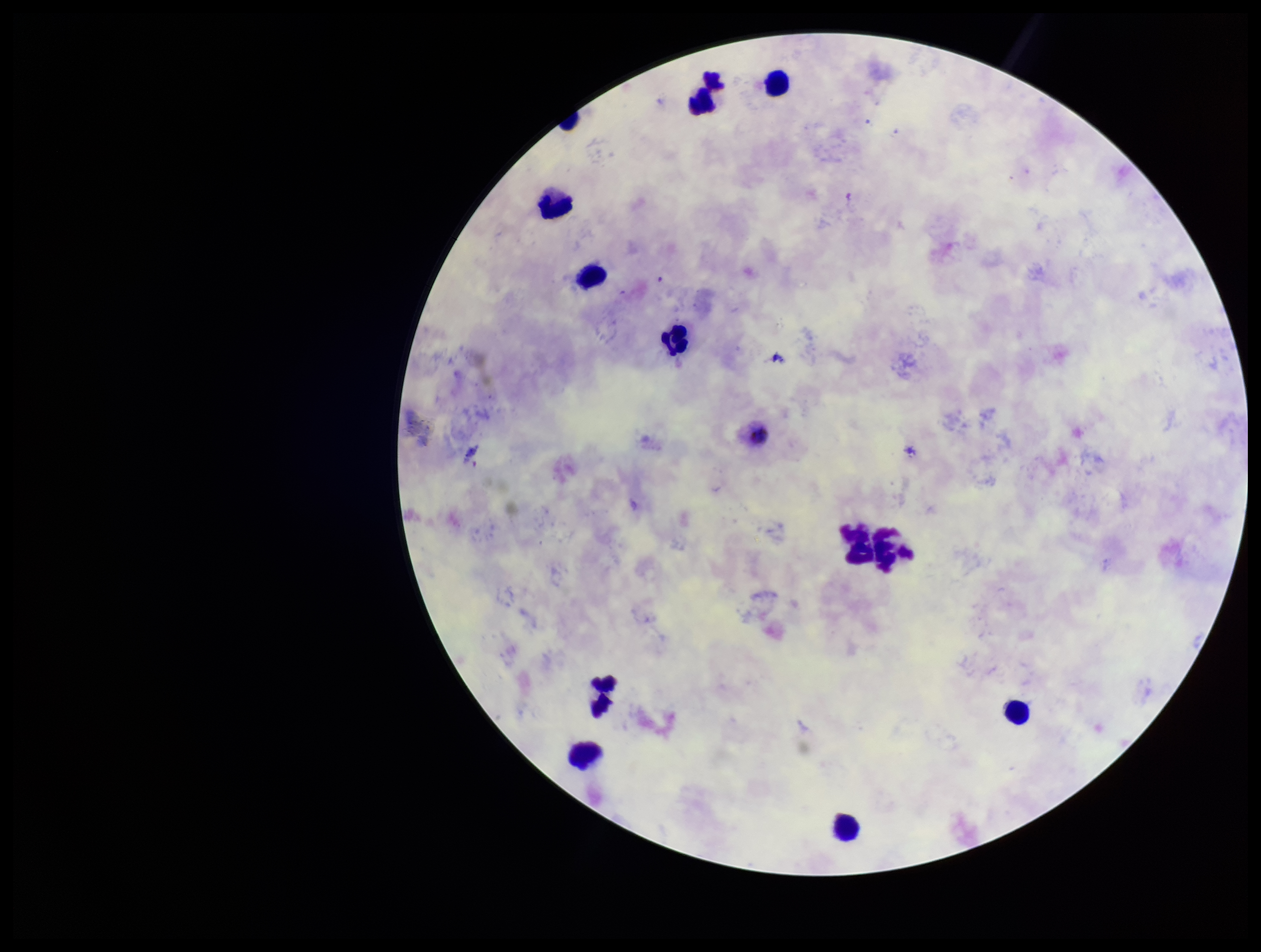
preparation = thick smear
species reported for this patient = Plasmodium vivax
leukocyte count = 13
capture = smartphone photograph through the microscope eyepiece
Plasmodium parasites = none seen
field of view = single
patient malaria status = positive
stain = Giemsa
image size = 1261×952 pixels
parasite count = 0